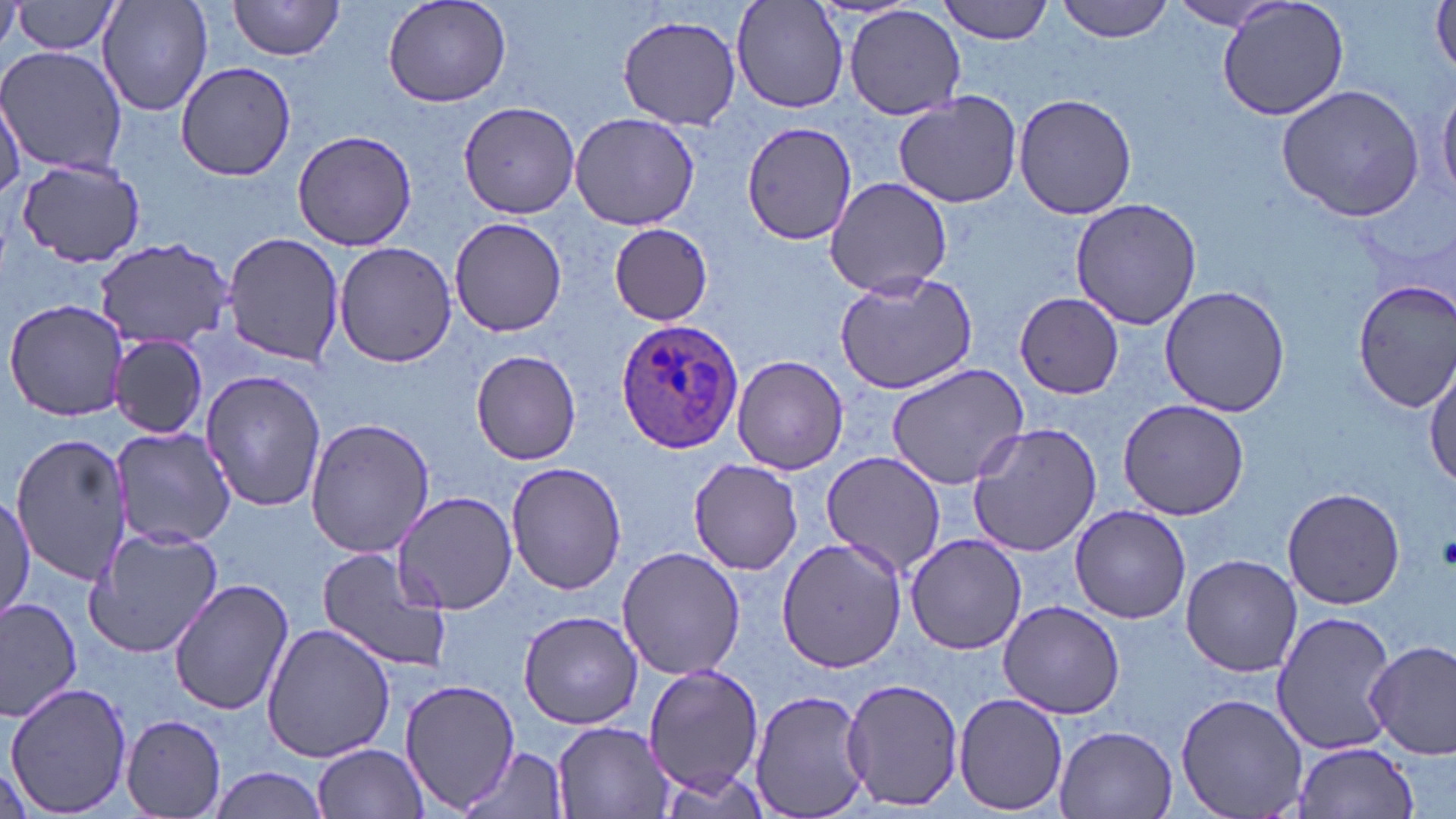

Approximate bounding boxes as [x1, y1, x2, y2] in pixels. Plasmodium ovale-infected red blood cell locations: [615, 320, 742, 453]. Platelet locations: [1437, 533, 1456, 568]. Uninfected red blood cell locations: [97, 0, 214, 117], [228, 0, 347, 61], [382, 0, 512, 108], [939, 0, 1056, 44], [1056, 0, 1175, 43], [1215, 0, 1353, 122], [733, 1, 849, 114], [1431, 1, 1456, 78], [1, 2, 22, 53], [12, 2, 123, 57], [1165, 3, 1290, 31], [844, 5, 965, 119], [616, 13, 742, 130], [0, 45, 127, 175], [176, 60, 296, 181], [1276, 85, 1428, 222], [1437, 86, 1456, 202], [892, 90, 1025, 208], [1, 93, 24, 196], [1014, 93, 1136, 219], [458, 101, 582, 220], [569, 112, 700, 232], [740, 119, 856, 247], [291, 130, 417, 250], [14, 157, 146, 267], [824, 177, 954, 296], [1070, 197, 1203, 330], [449, 214, 567, 338], [606, 223, 713, 325], [220, 232, 344, 368], [95, 240, 233, 348], [333, 241, 457, 369], [831, 269, 980, 394], [1353, 278, 1456, 413], [1160, 283, 1289, 418], [1014, 290, 1125, 399], [4, 298, 127, 422], [108, 336, 210, 438], [470, 351, 582, 465], [733, 354, 848, 474], [1426, 359, 1456, 489], [885, 362, 1029, 491], [198, 366, 329, 514], [1119, 398, 1248, 520], [305, 417, 436, 558], [966, 422, 1101, 557], [110, 424, 236, 549], [10, 431, 131, 586], [819, 449, 949, 576], [687, 459, 804, 574], [506, 460, 628, 594], [1281, 487, 1405, 609], [393, 490, 519, 613], [0, 496, 35, 624], [1069, 505, 1193, 624], [85, 526, 224, 657], [905, 534, 1027, 655], [777, 536, 909, 672], [616, 545, 746, 682], [316, 546, 451, 674], [1181, 554, 1302, 677], [168, 578, 294, 716], [0, 594, 82, 721], [997, 601, 1126, 718], [518, 610, 645, 729], [1274, 613, 1393, 754], [261, 623, 399, 764], [1365, 640, 1456, 759], [644, 664, 765, 792], [841, 676, 964, 811], [399, 677, 521, 814], [5, 680, 132, 816], [749, 688, 873, 816], [954, 690, 1071, 814], [1175, 693, 1310, 819], [119, 713, 228, 817], [552, 720, 672, 818], [1053, 724, 1179, 818], [1292, 741, 1420, 817], [314, 743, 428, 818], [457, 748, 572, 818], [207, 766, 334, 818]. Slide-level diagnosis: Plasmodium ovale. Image is 1456×819 pixels. May-Grünwald-Giemsa-stained preparation. Thin blood film. 1000x magnification. One field of a larger specimen. Optical microscopy.